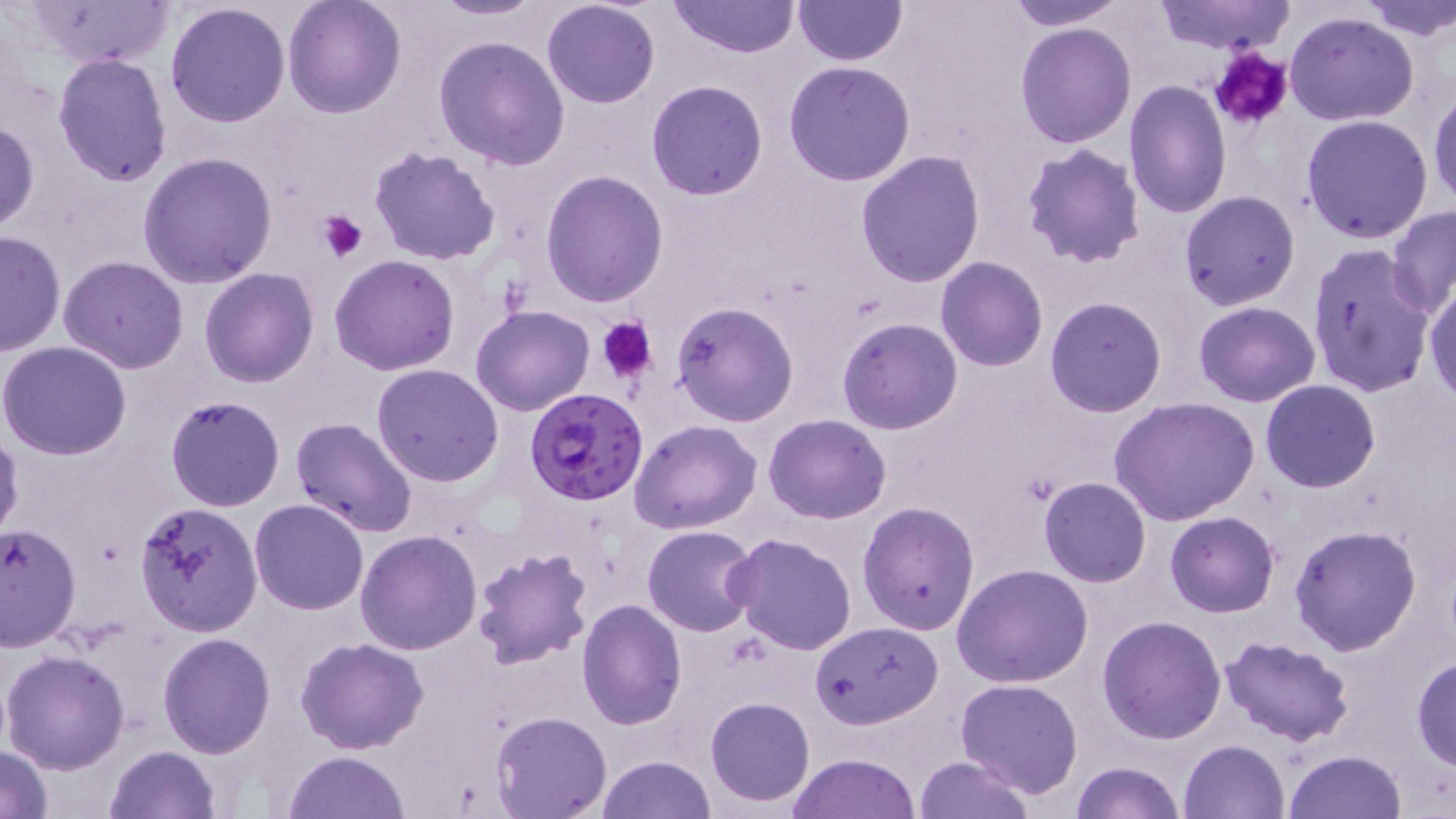

slide-level diagnosis = Plasmodium falciparum
magnification = 1000x
field of view = single
image size = 1456×819 pixels
uninfected red blood cell locations = approximate bounding boxes as named x1/y1/x2/y2 corners in pixels: (x1=27, y1=0, x2=175, y2=70), (x1=283, y1=0, x2=407, y2=118), (x1=431, y1=0, x2=544, y2=20), (x1=541, y1=0, x2=663, y2=109), (x1=669, y1=0, x2=801, y2=59), (x1=792, y1=0, x2=907, y2=66), (x1=1001, y1=0, x2=1133, y2=29), (x1=1153, y1=0, x2=1298, y2=53), (x1=1353, y1=0, x2=1454, y2=39), (x1=165, y1=3, x2=292, y2=129), (x1=1284, y1=12, x2=1419, y2=127), (x1=1015, y1=22, x2=1137, y2=149), (x1=433, y1=37, x2=570, y2=171), (x1=52, y1=52, x2=172, y2=188), (x1=785, y1=61, x2=916, y2=186), (x1=1124, y1=79, x2=1232, y2=219), (x1=645, y1=80, x2=769, y2=200), (x1=1428, y1=89, x2=1456, y2=208), (x1=1302, y1=113, x2=1434, y2=244), (x1=0, y1=120, x2=38, y2=235), (x1=1021, y1=143, x2=1146, y2=266), (x1=369, y1=145, x2=501, y2=265), (x1=855, y1=150, x2=986, y2=287), (x1=136, y1=151, x2=280, y2=288), (x1=541, y1=169, x2=670, y2=307), (x1=1179, y1=190, x2=1301, y2=311), (x1=1388, y1=205, x2=1456, y2=316), (x1=0, y1=228, x2=64, y2=357), (x1=1306, y1=243, x2=1437, y2=398), (x1=330, y1=253, x2=460, y2=375), (x1=58, y1=256, x2=188, y2=373), (x1=936, y1=257, x2=1048, y2=372), (x1=200, y1=268, x2=319, y2=387), (x1=1425, y1=281, x2=1456, y2=405), (x1=1044, y1=296, x2=1167, y2=417), (x1=1193, y1=301, x2=1320, y2=407), (x1=672, y1=302, x2=799, y2=427), (x1=471, y1=305, x2=596, y2=417), (x1=838, y1=317, x2=963, y2=434), (x1=0, y1=341, x2=132, y2=461), (x1=371, y1=363, x2=505, y2=486), (x1=1260, y1=379, x2=1381, y2=493), (x1=165, y1=396, x2=287, y2=512), (x1=1109, y1=396, x2=1260, y2=525), (x1=765, y1=414, x2=892, y2=524), (x1=290, y1=417, x2=418, y2=539), (x1=630, y1=420, x2=763, y2=534), (x1=0, y1=423, x2=22, y2=548), (x1=1039, y1=477, x2=1151, y2=587), (x1=249, y1=498, x2=368, y2=614), (x1=134, y1=500, x2=263, y2=637), (x1=858, y1=502, x2=979, y2=634), (x1=1165, y1=512, x2=1280, y2=617), (x1=0, y1=523, x2=82, y2=651), (x1=1289, y1=523, x2=1423, y2=655), (x1=642, y1=525, x2=761, y2=636), (x1=355, y1=530, x2=482, y2=654), (x1=727, y1=533, x2=857, y2=657), (x1=472, y1=547, x2=594, y2=669), (x1=953, y1=563, x2=1094, y2=688), (x1=576, y1=599, x2=687, y2=730), (x1=1096, y1=614, x2=1226, y2=743), (x1=809, y1=621, x2=943, y2=728), (x1=156, y1=632, x2=275, y2=758), (x1=1220, y1=634, x2=1356, y2=747), (x1=296, y1=638, x2=429, y2=754), (x1=2, y1=650, x2=130, y2=774), (x1=1411, y1=654, x2=1456, y2=770), (x1=956, y1=676, x2=1085, y2=798), (x1=706, y1=696, x2=816, y2=806), (x1=491, y1=709, x2=613, y2=817), (x1=1178, y1=739, x2=1290, y2=819), (x1=1, y1=745, x2=53, y2=819), (x1=103, y1=745, x2=221, y2=819), (x1=1283, y1=750, x2=1407, y2=819), (x1=284, y1=751, x2=411, y2=819), (x1=789, y1=753, x2=921, y2=819), (x1=597, y1=755, x2=716, y2=819), (x1=914, y1=755, x2=1035, y2=818), (x1=1072, y1=761, x2=1183, y2=819)
modality = light microscopy
Plasmodium falciparum-infected red blood cell locations = approximate bounding boxes as named x1/y1/x2/y2 corners in pixels: (x1=525, y1=387, x2=651, y2=506)
stain = May-Grünwald-Giemsa
platelet locations = approximate bounding boxes as named x1/y1/x2/y2 corners in pixels: (x1=1208, y1=46, x2=1295, y2=132), (x1=317, y1=210, x2=367, y2=263), (x1=598, y1=316, x2=658, y2=384)
preparation = thin blood film